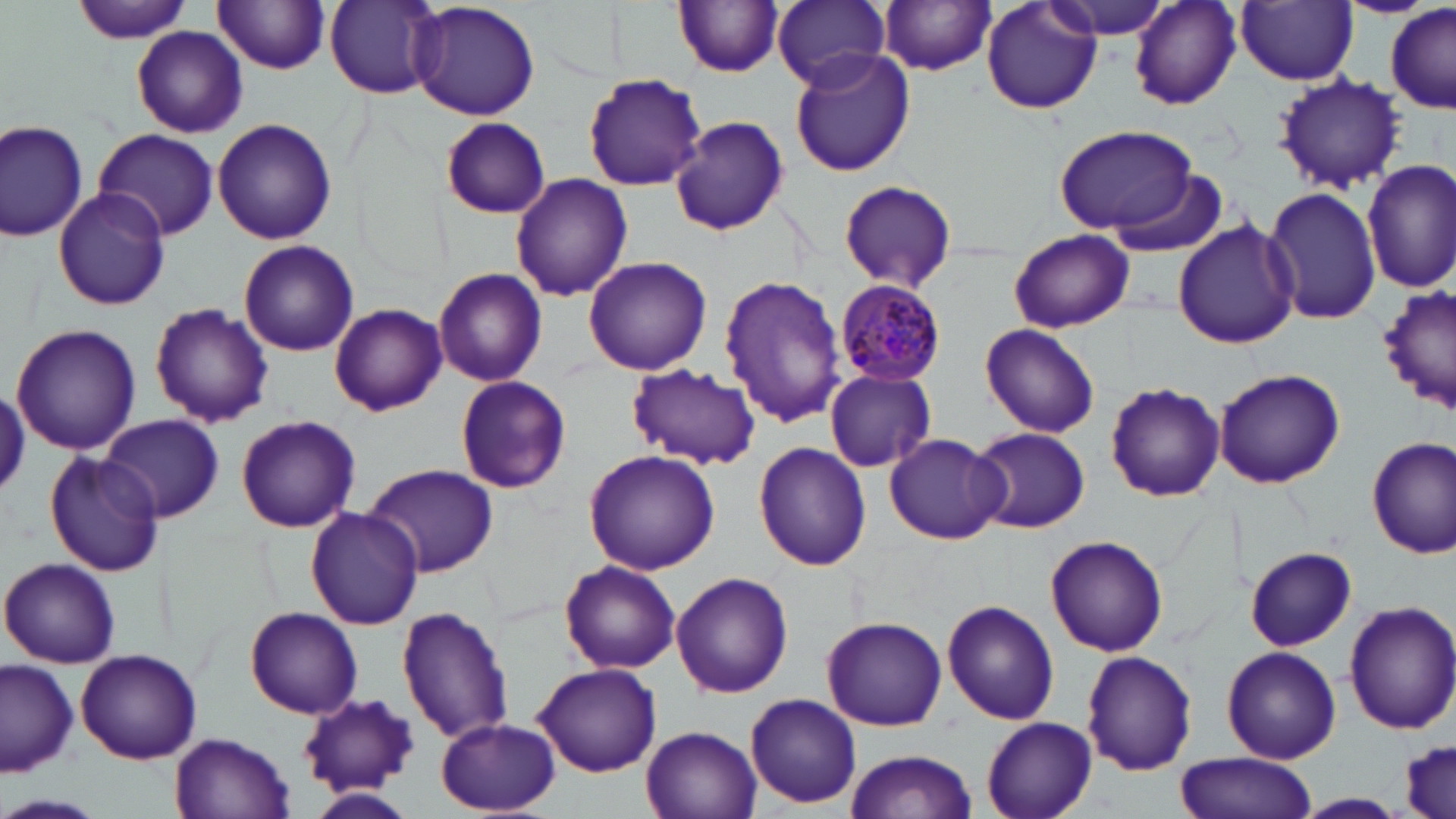
{
  "slide_level_diagnosis": "Plasmodium malariae",
  "image_size": "1456×819 pixels",
  "stain": "May-Grünwald-Giemsa",
  "preparation": "thin blood smear",
  "plasmodium_malariae_infected_red_blood_cell_locations": "approximate bounding boxes as named x1/y1/x2/y2 corners in pixels: (x1=833, y1=283, x2=949, y2=385)",
  "uninfected_red_blood_cell_locations": "approximate bounding boxes as named x1/y1/x2/y2 corners in pixels: (x1=70, y1=0, x2=194, y2=45), (x1=675, y1=0, x2=784, y2=78), (x1=772, y1=0, x2=892, y2=91), (x1=982, y1=0, x2=1101, y2=116), (x1=1044, y1=0, x2=1175, y2=41), (x1=213, y1=1, x2=334, y2=74), (x1=325, y1=1, x2=444, y2=99), (x1=409, y1=1, x2=541, y2=121), (x1=878, y1=1, x2=996, y2=75), (x1=1131, y1=2, x2=1243, y2=109), (x1=1237, y1=2, x2=1358, y2=86), (x1=1386, y1=5, x2=1456, y2=115), (x1=131, y1=26, x2=248, y2=138), (x1=788, y1=48, x2=916, y2=177), (x1=582, y1=73, x2=706, y2=190), (x1=1273, y1=73, x2=1404, y2=193), (x1=671, y1=115, x2=789, y2=237), (x1=442, y1=117, x2=549, y2=218), (x1=0, y1=118, x2=91, y2=243), (x1=213, y1=118, x2=338, y2=246), (x1=1053, y1=124, x2=1201, y2=237), (x1=93, y1=127, x2=218, y2=241), (x1=1362, y1=159, x2=1456, y2=292), (x1=511, y1=173, x2=632, y2=300), (x1=839, y1=178, x2=956, y2=295), (x1=1264, y1=187, x2=1383, y2=326), (x1=53, y1=188, x2=171, y2=311), (x1=1172, y1=220, x2=1301, y2=349), (x1=1007, y1=229, x2=1134, y2=333), (x1=239, y1=240, x2=359, y2=356), (x1=584, y1=254, x2=713, y2=375), (x1=433, y1=268, x2=548, y2=387), (x1=719, y1=275, x2=847, y2=427), (x1=1376, y1=285, x2=1454, y2=413), (x1=149, y1=302, x2=273, y2=428), (x1=330, y1=303, x2=446, y2=416), (x1=12, y1=323, x2=141, y2=455), (x1=980, y1=323, x2=1101, y2=437), (x1=627, y1=364, x2=762, y2=469), (x1=1214, y1=367, x2=1347, y2=489), (x1=824, y1=368, x2=937, y2=471), (x1=454, y1=376, x2=571, y2=494), (x1=1104, y1=383, x2=1225, y2=503), (x1=103, y1=414, x2=224, y2=523), (x1=235, y1=415, x2=362, y2=533), (x1=970, y1=427, x2=1090, y2=534), (x1=882, y1=433, x2=1009, y2=545), (x1=1366, y1=435, x2=1455, y2=558), (x1=753, y1=442, x2=873, y2=572), (x1=582, y1=448, x2=721, y2=575), (x1=42, y1=449, x2=163, y2=577), (x1=363, y1=462, x2=499, y2=578), (x1=304, y1=505, x2=424, y2=630), (x1=1046, y1=537, x2=1168, y2=656), (x1=1245, y1=547, x2=1357, y2=650), (x1=0, y1=557, x2=123, y2=668), (x1=558, y1=560, x2=682, y2=674), (x1=4, y1=561, x2=102, y2=773), (x1=671, y1=572, x2=793, y2=698), (x1=941, y1=600, x2=1059, y2=725), (x1=1343, y1=601, x2=1456, y2=734), (x1=397, y1=606, x2=514, y2=744), (x1=244, y1=608, x2=361, y2=718), (x1=821, y1=614, x2=947, y2=730), (x1=1221, y1=645, x2=1341, y2=764), (x1=76, y1=649, x2=201, y2=764), (x1=1081, y1=650, x2=1198, y2=775), (x1=1, y1=658, x2=78, y2=778), (x1=533, y1=663, x2=662, y2=776), (x1=744, y1=692, x2=863, y2=810), (x1=297, y1=693, x2=421, y2=796), (x1=981, y1=717, x2=1098, y2=819), (x1=437, y1=718, x2=561, y2=813), (x1=639, y1=723, x2=764, y2=819), (x1=171, y1=733, x2=293, y2=818), (x1=1400, y1=738, x2=1456, y2=819), (x1=844, y1=750, x2=980, y2=819), (x1=1174, y1=753, x2=1316, y2=819), (x1=307, y1=788, x2=414, y2=819), (x1=0, y1=793, x2=109, y2=819), (x1=1296, y1=793, x2=1409, y2=817)",
  "field_of_view": "one of a larger specimen",
  "modality": "optical microscopy",
  "magnification": "1000x"
}